Report the malaria status of this cell.
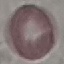
It is uninfected.

Cell patch, automatically extracted from a larger field of view and resized to 64 × 64 pixels. Giemsa stain. Photographed with a smartphone camera at the microscope eyepiece. Thin blood smear.